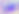
Summary:
  - Identification: Toxoplasma gondii
  - Modality: photomicrograph
  - Magnification: 400x